Assess this cell for malaria.
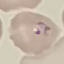
Parasitized.

Giemsa-stained preparation. Thin blood film. Acquired by smartphone through the microscope eyepiece. Cell patch, automatically extracted from a larger field of view and resized to 64 × 64 pixels.